Name the parasite shown.
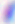

This is Toxoplasma gondii.

Summary:
  - Modality: photomicrograph
  - Magnification: 400x